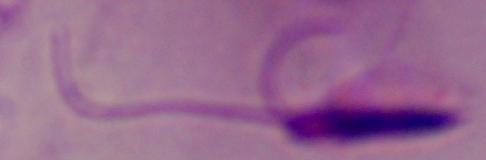
A Leishmania parasite is seen. 1000x magnification. Micrograph.